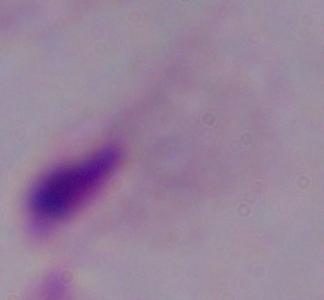 Micrograph. A trichomonad is shown. Captured at 1000x magnification.